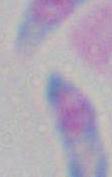
Summary:
  - Identification: Toxoplasma gondii
  - Magnification: 1000x
  - Modality: photomicrograph